Identify the parasite.
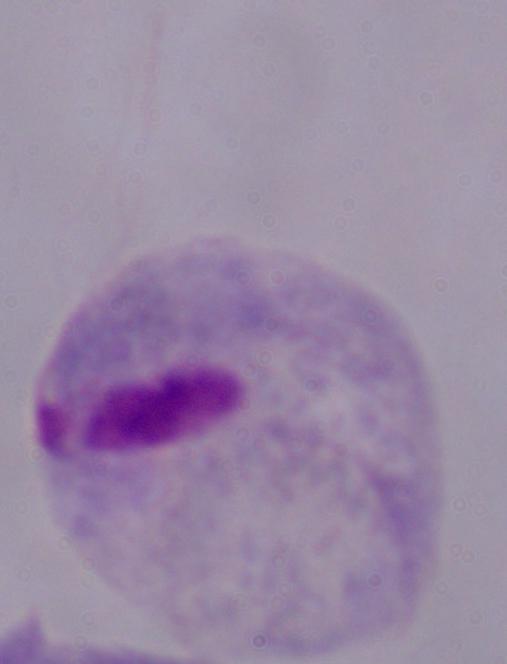

A trichomonad.

Summary:
  - Modality: micrograph
  - Magnification: 1000x